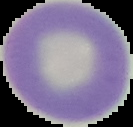

image type = cell region segmented out of the field of view; surrounding area masked to black
result = no Plasmodium parasites detected
preparation = thin blood film
image size = 133×127 pixels